Look for Plasmodium parasites.
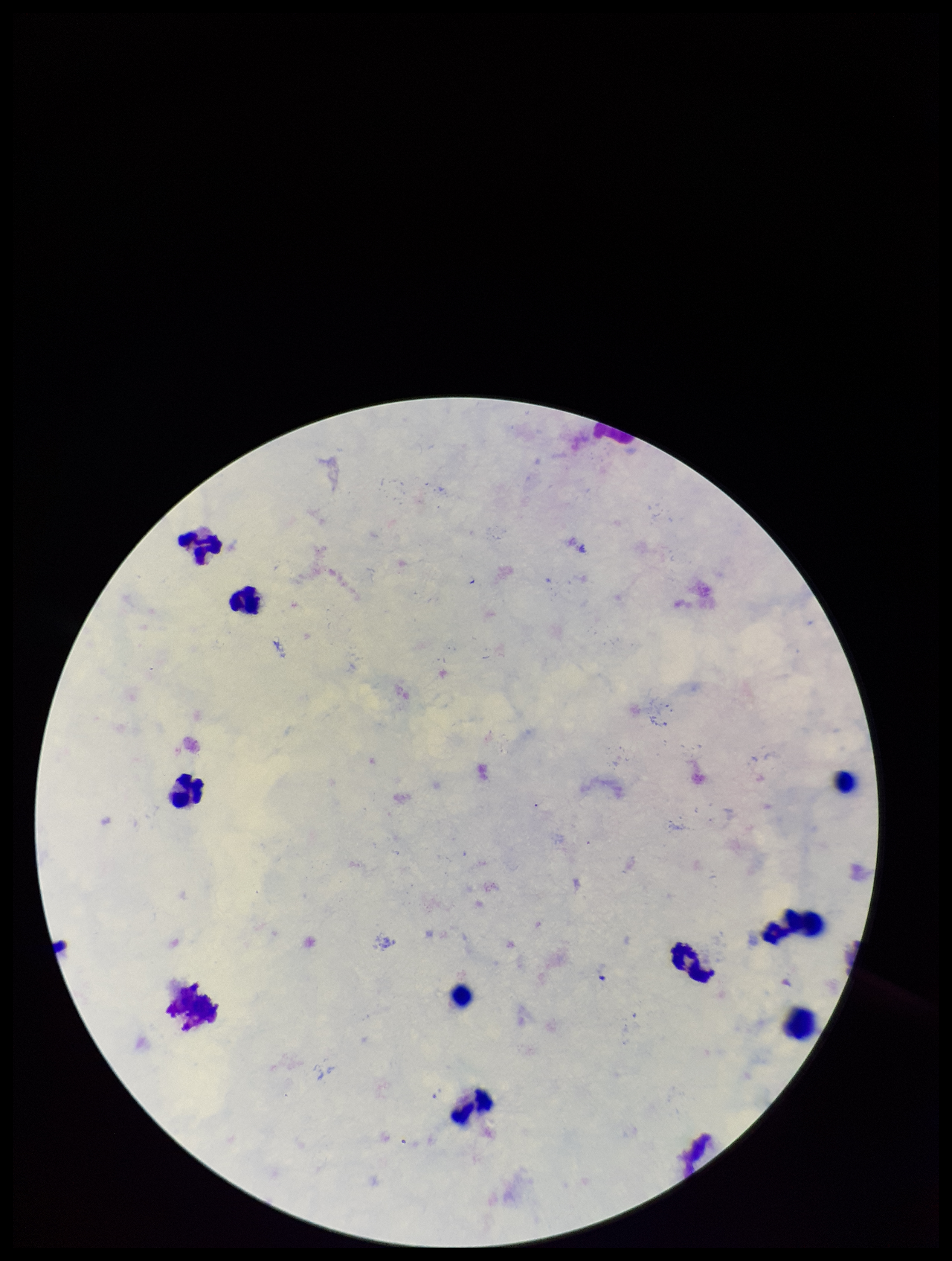

Detected.

Patient malaria status: infected. Image is 952×1261 pixels. Giemsa stain. Leukocyte count: 10. Preparation: thick smear. One field from this slide. Smartphone photograph taken through the eyepiece of a microscope. Parasite count: 1. Species reported for this patient: Plasmodium falciparum.